State the blood parasite species.
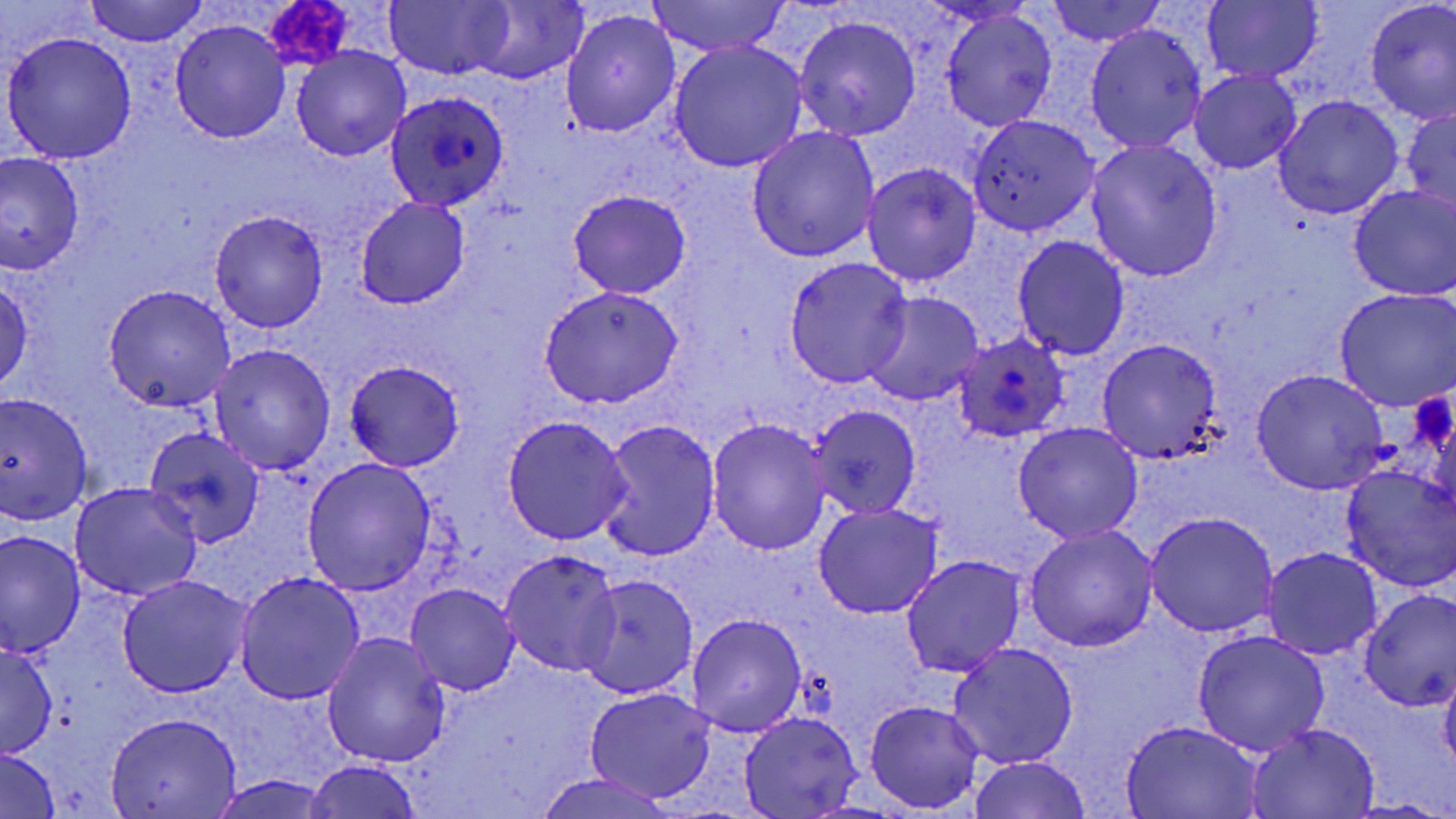
Plasmodium ovale.

Approximate bounding boxes as [x1, y1, x2, y2] in pixels. Uninfected red blood cell locations: [86, 0, 207, 46], [645, 0, 794, 57], [1045, 0, 1165, 47], [1364, 0, 1456, 122], [382, 1, 514, 80], [466, 1, 585, 84], [1201, 2, 1323, 84], [561, 9, 681, 138], [940, 9, 1056, 131], [793, 15, 921, 140], [170, 19, 290, 143], [1086, 25, 1207, 153], [4, 30, 137, 163], [670, 43, 807, 171], [291, 46, 410, 162], [1191, 71, 1301, 174], [1272, 96, 1404, 218], [1401, 107, 1456, 214], [966, 113, 1101, 237], [746, 126, 880, 263], [1087, 138, 1223, 282], [2, 153, 84, 273], [862, 163, 981, 287], [1349, 183, 1456, 301], [567, 189, 691, 299], [354, 198, 471, 309], [210, 209, 328, 333], [1012, 236, 1130, 360], [783, 256, 912, 388], [1, 275, 32, 393], [102, 285, 239, 411], [539, 286, 684, 407], [1334, 289, 1455, 410], [863, 291, 985, 407], [1098, 338, 1224, 463], [209, 343, 335, 474], [345, 360, 463, 470], [1251, 370, 1389, 494], [0, 392, 94, 523], [808, 404, 922, 521], [501, 415, 632, 545], [597, 419, 720, 562], [706, 419, 830, 558], [1013, 422, 1143, 544], [145, 425, 267, 548], [302, 459, 435, 594], [1338, 463, 1456, 591], [69, 483, 202, 602], [813, 503, 943, 618], [1143, 514, 1278, 637], [1024, 525, 1157, 651], [1, 533, 84, 657], [1261, 546, 1384, 660], [500, 552, 623, 675], [900, 556, 1026, 677], [233, 571, 366, 705], [579, 574, 697, 699], [117, 576, 254, 696], [406, 582, 519, 694], [1359, 591, 1456, 708], [687, 613, 807, 738], [1191, 630, 1331, 756], [322, 631, 451, 768], [0, 642, 57, 758], [946, 643, 1080, 769], [1439, 665, 1456, 773], [585, 688, 714, 803], [864, 700, 986, 814], [739, 711, 862, 818], [104, 713, 242, 818], [1120, 719, 1263, 818], [1245, 723, 1380, 817], [0, 748, 61, 819], [966, 756, 1093, 819], [305, 760, 423, 819], [534, 771, 679, 818], [209, 774, 334, 818]. Platelet locations: [269, 1, 353, 66], [1411, 391, 1455, 456]. Plasmodium ovale-infected red blood cell locations: [385, 87, 509, 209], [956, 334, 1069, 443]. One field of a larger specimen. Image is 1456×819 pixels. May-Grünwald-Giemsa-stained preparation. Thin blood film. Captured at 1000x magnification. Light microscopy.